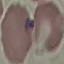
Summary:
  - Malaria status: parasitized
  - Preparation: thin blood smear
  - Capture: smartphone through the microscope eyepiece
  - Image type: automatically extracted cell patch, resized to 64 × 64 pixels
  - Stain: Giemsa